Locate every blood parasite and identify its species.
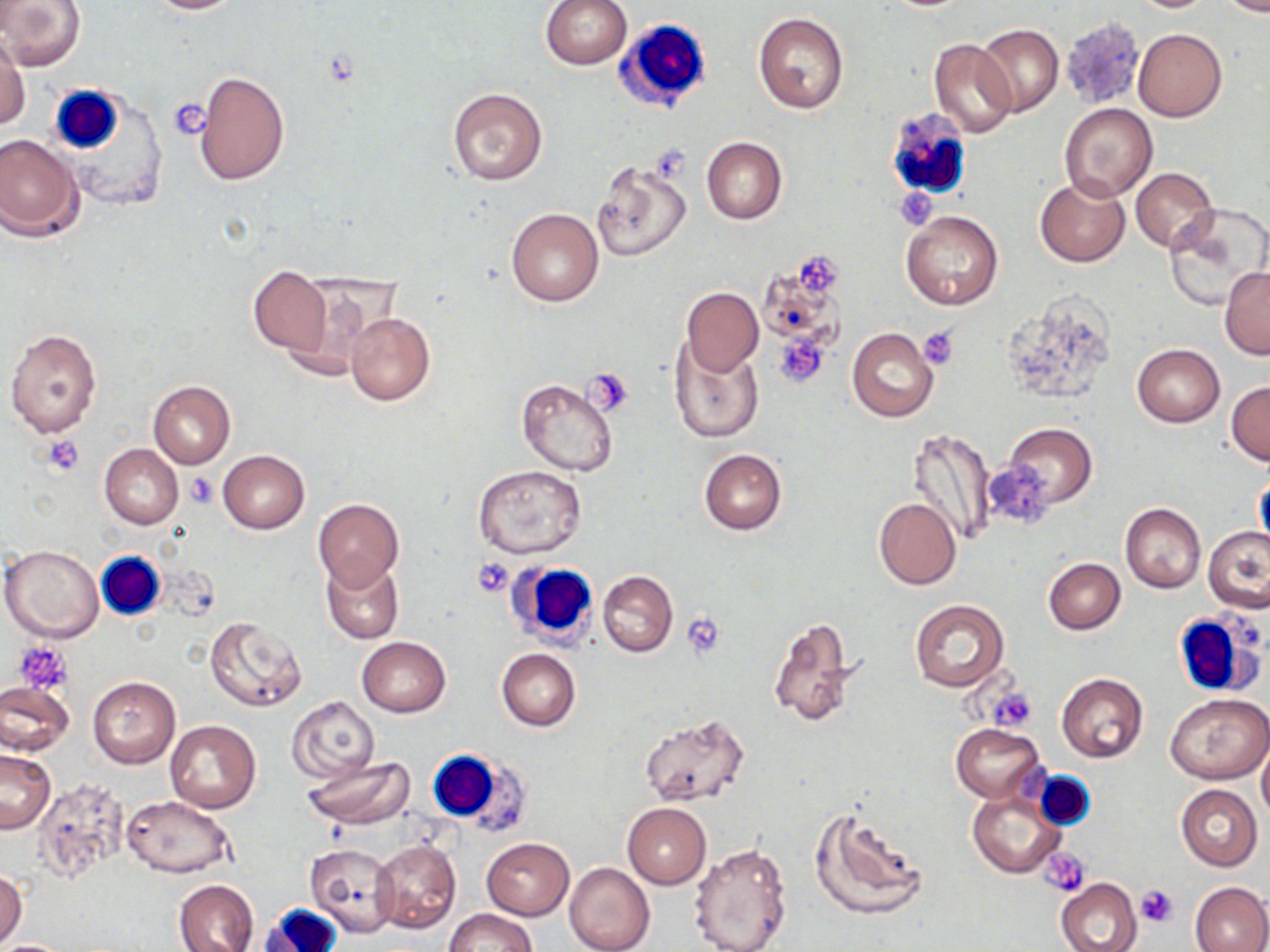
No blood parasites observed.

slide-level diagnosis = negative for blood parasites
white blood cell locations = approximate bounding boxes as (x1, y1, x2, y2) in pixels: (613, 18, 713, 113), (48, 86, 126, 153), (885, 108, 975, 200), (97, 551, 167, 619), (511, 564, 596, 648), (1173, 610, 1266, 698), (432, 751, 530, 838), (256, 904, 343, 952)
preparation = thin blood smear
uninfected red blood cell locations = approximate bounding boxes as (x1, y1, x2, y2) in pixels: (1, 0, 86, 69), (142, 0, 247, 15), (540, 0, 633, 71), (1124, 0, 1220, 13), (1214, 0, 1270, 17), (753, 12, 850, 114), (975, 22, 1063, 117), (1133, 28, 1226, 121), (1, 39, 29, 132), (929, 39, 1017, 138), (195, 69, 289, 186), (447, 86, 548, 186), (1058, 104, 1158, 202), (0, 134, 85, 242), (702, 137, 786, 224), (592, 160, 692, 264), (1130, 168, 1218, 252), (1035, 176, 1130, 267), (1164, 204, 1270, 309), (505, 207, 604, 307), (901, 210, 1003, 310), (248, 267, 331, 354), (1220, 268, 1270, 359), (281, 279, 382, 380), (682, 287, 763, 375), (344, 311, 435, 406), (5, 328, 103, 439), (848, 329, 938, 422), (670, 338, 763, 444), (1131, 344, 1225, 427), (516, 377, 618, 475), (1227, 380, 1270, 465), (148, 381, 235, 468), (1003, 423, 1096, 508), (907, 428, 995, 547), (99, 444, 183, 530), (699, 448, 786, 534), (217, 450, 310, 534), (474, 466, 587, 560), (1253, 473, 1270, 559), (314, 497, 403, 591), (873, 498, 960, 590), (1120, 502, 1206, 593), (1204, 526, 1270, 614), (1, 544, 105, 643), (322, 558, 404, 644), (1043, 558, 1125, 634), (598, 571, 678, 657), (909, 598, 1009, 693), (205, 616, 307, 713), (768, 617, 859, 728), (356, 636, 451, 717), (496, 649, 580, 730), (1057, 673, 1148, 764), (87, 676, 180, 768), (0, 680, 73, 754), (1166, 691, 1269, 784), (288, 695, 379, 785), (638, 715, 748, 808), (166, 720, 260, 813), (951, 723, 1045, 802), (1257, 740, 1270, 823), (0, 749, 56, 833), (301, 757, 413, 828), (33, 776, 133, 882), (1176, 785, 1262, 871), (968, 791, 1065, 879), (121, 796, 236, 879), (622, 803, 711, 888), (809, 808, 928, 922), (481, 838, 574, 919), (372, 839, 461, 933), (688, 842, 793, 952), (305, 843, 398, 937), (564, 862, 654, 952), (0, 869, 27, 948), (1056, 877, 1142, 952), (173, 879, 260, 952), (1189, 881, 1270, 952), (444, 907, 536, 952), (2, 940, 71, 952)
image size = 1270×952 pixels
platelet locations = approximate bounding boxes as (x1, y1, x2, y2) in pixels: (167, 97, 214, 140), (797, 251, 844, 299), (917, 325, 960, 369), (774, 334, 828, 387), (585, 369, 636, 416), (41, 436, 86, 475), (187, 472, 220, 508), (470, 557, 516, 597), (681, 613, 725, 658), (13, 639, 74, 694), (988, 688, 1037, 732), (1042, 849, 1090, 895), (1135, 885, 1178, 927)
modality = light microscopy
magnification = 1000x
stain = May-Grünwald-Giemsa
field of view = one of a larger specimen